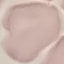

Summary:
  - Malaria status: uninfected
  - Preparation: thin smear
  - Stain: Giemsa
  - Capture: smartphone through the microscope eyepiece
  - Image type: cell patch, automatically extracted from a larger field of view and resized to 64 × 64 pixels